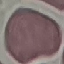
Result: no malaria parasites detected. Cell patch, automatically extracted from a larger field of view and resized to 64 × 64 pixels. Giemsa stain. Thin blood film. Photographed with a smartphone camera at the microscope eyepiece.